State which cell type is depicted.
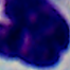
This is a leukocyte.

Summary:
  - Magnification: 1000x
  - Modality: photomicrograph